Assess this cell for malaria.
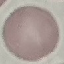
Uninfected.

Summary:
  - Stain: Giemsa
  - Preparation: thin smear
  - Image type: automatically extracted cell patch, resized to 64 × 64 pixels
  - Capture: smartphone through the microscope eyepiece